Assess this cell for malaria.
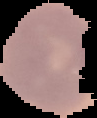
It is uninfected.

Summary:
  - Image size: 97×118 pixels
  - Image type: segmented cell region on a black background
  - Preparation: thin blood film